Describe the morphology of the red blood cells.
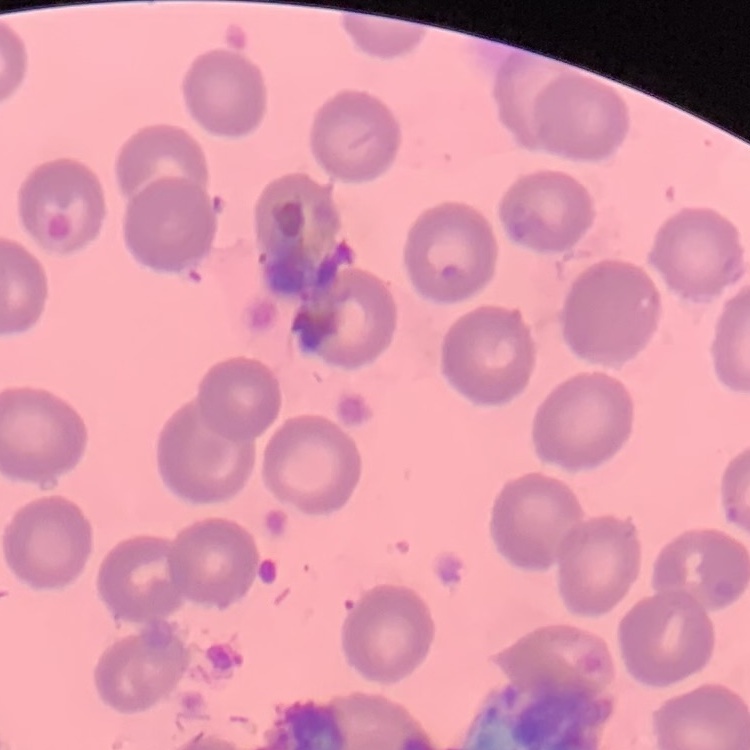

No rouleaux formation.

Thin blood smear. Stained with either Field's or Giemsa. One tile cut from a larger photomicrograph.